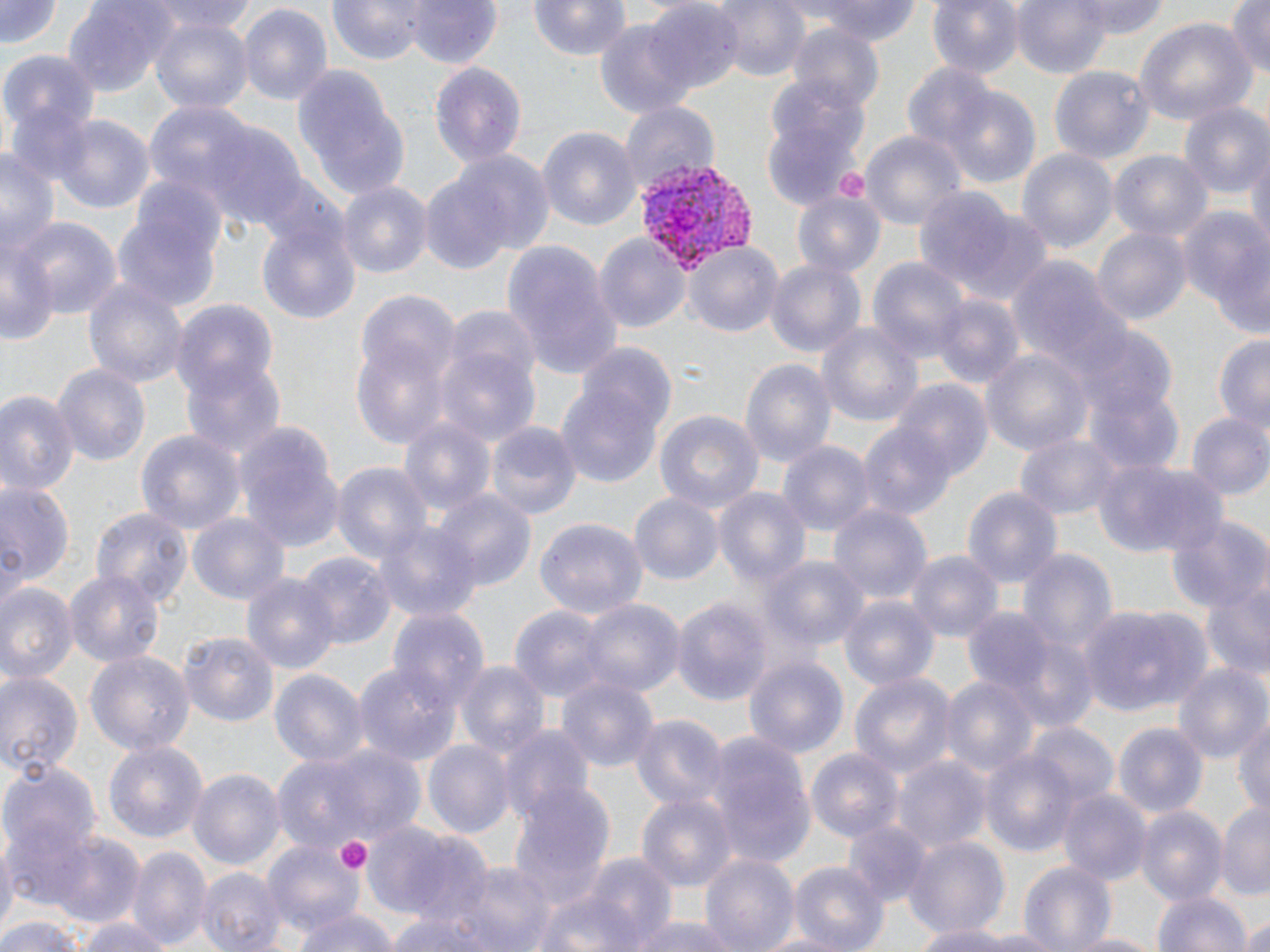
Plasmodium vivax-infected red blood cell locations = approximate bounding boxes as (x1, y1, x2, y2) in pixels: (636, 159, 757, 271)
slide-level diagnosis = Plasmodium vivax
stain = May-Grünwald-Giemsa
modality = light microscopy
image size = 1270×952 pixels
uninfected red blood cell locations = approximate bounding boxes as (x1, y1, x2, y2) in pixels: (0, 0, 62, 50), (147, 0, 255, 39), (326, 0, 425, 67), (528, 0, 631, 62), (710, 0, 809, 82), (810, 0, 922, 47), (928, 0, 1023, 81), (1012, 0, 1118, 81), (1072, 0, 1171, 37), (1226, 0, 1270, 78), (63, 1, 179, 94), (407, 1, 500, 70), (644, 2, 742, 95), (236, 3, 335, 107), (148, 15, 251, 113), (1134, 17, 1255, 125), (595, 20, 697, 121), (783, 25, 885, 111), (2, 50, 102, 136), (902, 60, 1010, 172), (427, 61, 527, 169), (1049, 64, 1153, 165), (294, 73, 409, 202), (941, 86, 1042, 193), (617, 100, 720, 197), (1179, 102, 1270, 202), (144, 103, 257, 208), (9, 104, 97, 191), (762, 112, 865, 207), (50, 114, 152, 213), (206, 119, 309, 232), (537, 127, 642, 230), (859, 131, 966, 228), (0, 146, 58, 266), (435, 148, 554, 264), (1018, 149, 1118, 258), (1110, 150, 1212, 244), (1245, 150, 1270, 254), (337, 180, 432, 282), (912, 187, 1031, 294), (791, 191, 885, 278), (113, 196, 221, 314), (1178, 205, 1269, 325), (14, 215, 120, 321), (257, 217, 361, 323), (1091, 224, 1193, 326), (595, 231, 690, 336), (1, 234, 55, 347), (496, 238, 625, 383), (681, 240, 784, 338), (766, 257, 866, 360), (1007, 257, 1135, 385), (867, 258, 972, 369), (81, 276, 188, 390), (354, 289, 463, 447), (928, 295, 1023, 391), (170, 299, 277, 399), (817, 321, 922, 433), (1081, 328, 1178, 422), (1213, 334, 1270, 430), (435, 341, 541, 448), (577, 344, 681, 447), (980, 347, 1094, 460), (739, 357, 836, 470), (181, 358, 286, 462), (52, 363, 151, 467), (555, 379, 664, 491), (893, 381, 992, 482), (1086, 384, 1183, 476), (0, 386, 79, 498), (654, 409, 764, 516), (1187, 412, 1270, 503), (400, 418, 494, 519), (234, 420, 343, 553), (859, 421, 957, 523), (484, 423, 580, 524), (135, 429, 245, 537), (1013, 433, 1124, 519), (779, 440, 874, 540), (1092, 455, 1224, 557), (328, 461, 432, 568), (0, 474, 74, 597), (961, 484, 1063, 589), (714, 485, 814, 598), (432, 489, 536, 591), (628, 492, 723, 584), (829, 500, 933, 603), (90, 508, 190, 608), (1165, 512, 1270, 615), (189, 516, 288, 604), (373, 518, 481, 624), (536, 518, 647, 619), (1016, 547, 1120, 663), (908, 550, 1003, 644), (296, 551, 393, 652), (762, 554, 868, 652), (240, 568, 338, 673), (1198, 568, 1270, 682), (64, 571, 163, 666), (1, 580, 76, 681), (838, 594, 940, 695), (574, 597, 684, 699), (673, 598, 771, 705), (1079, 605, 1213, 718), (387, 607, 487, 714), (510, 607, 611, 702), (963, 608, 1057, 702), (180, 631, 279, 729), (87, 650, 193, 758), (744, 656, 850, 762), (353, 661, 458, 766), (455, 661, 547, 762), (1173, 665, 1267, 762), (0, 667, 84, 779), (269, 667, 369, 770), (848, 671, 955, 779), (942, 674, 1039, 779), (557, 675, 658, 776), (1233, 712, 1270, 820), (629, 713, 728, 812), (497, 723, 594, 823), (1026, 723, 1118, 813), (1116, 723, 1208, 821), (705, 733, 814, 869), (102, 740, 208, 848), (422, 740, 514, 840), (275, 741, 425, 849), (807, 743, 904, 845), (979, 747, 1079, 860), (896, 755, 991, 855), (3, 762, 101, 865), (188, 767, 283, 873), (510, 786, 614, 906), (1059, 788, 1151, 888), (636, 794, 735, 891), (1217, 800, 1270, 902), (1136, 806, 1226, 907), (840, 819, 932, 910), (363, 822, 475, 927), (0, 829, 19, 941), (51, 832, 145, 930), (904, 835, 1011, 937), (260, 839, 362, 943), (130, 845, 211, 950), (579, 853, 676, 952), (700, 853, 800, 952), (1020, 860, 1119, 952), (786, 861, 891, 949), (442, 863, 554, 950), (198, 866, 286, 952), (529, 889, 643, 952), (1155, 889, 1251, 952), (296, 908, 399, 952), (388, 911, 495, 952), (1235, 911, 1270, 952), (79, 915, 171, 952), (0, 916, 89, 952), (631, 916, 740, 952), (909, 919, 1038, 952), (1065, 930, 1160, 952)
preparation = thin blood film
field of view = one of a larger specimen
magnification = 1000x
platelet locations = approximate bounding boxes as (x1, y1, x2, y2) in pixels: (835, 169, 869, 201), (333, 835, 371, 873)